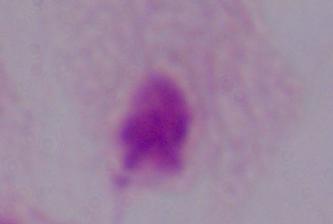

1000x magnification. A trichomonad is seen. Micrograph.